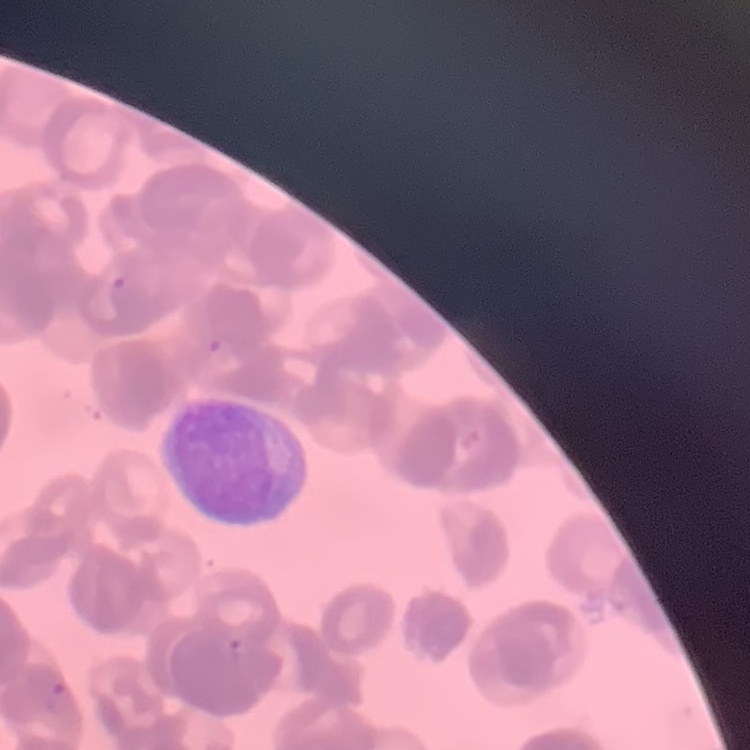

The red blood cells show rouleaux formation. Square crop of a larger photomicrograph. Stained with either Field's or Giemsa. Thin blood smear.